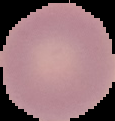
image_type: cell region segmented out of the field of view; surrounding area masked to black
malaria_status: uninfected
preparation: thin blood smear
image_size: 115×121 pixels